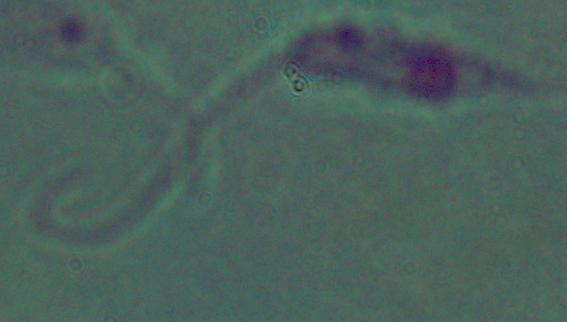
1000x magnification. A Leishmania parasite is shown. Micrograph.